Point out each leukocyte.
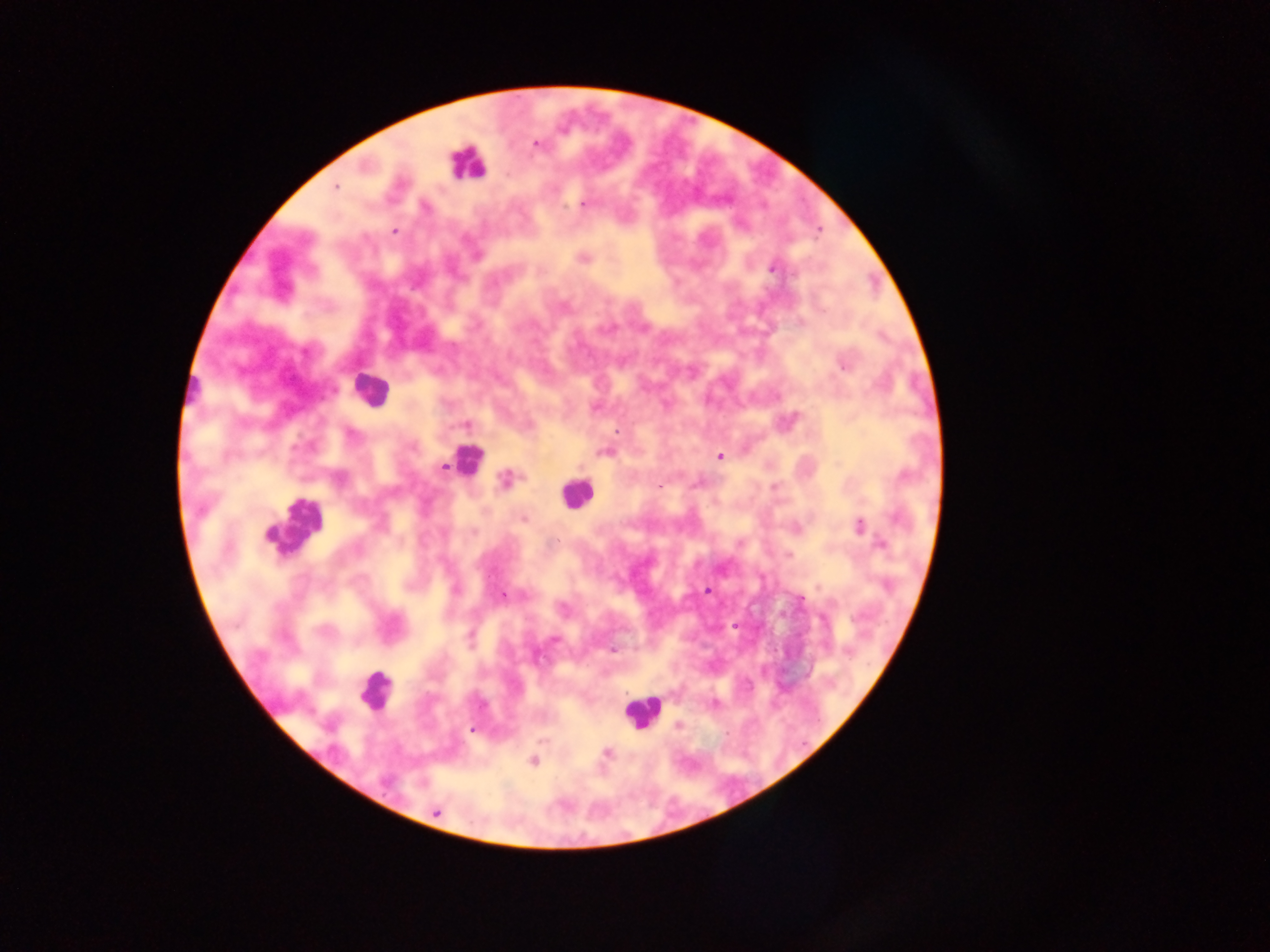

Approximate centers as {x, y} in pixels.
Leukocytes: {467, 163}, {371, 391}, {466, 460}, {575, 493}, {293, 528}, {375, 690}, {642, 712}.

Summary:
  - Plasmodium parasite locations: {536, 143}, {334, 187}, {582, 203}, {394, 231}, {477, 255}, {583, 257}, {773, 267}, {843, 363}, {595, 408}, {465, 424}, {617, 431}, {604, 451}, {719, 456}, {442, 468}, {506, 480}, {660, 487}, {774, 487}, {523, 518}, {859, 527}, {881, 543}, {708, 590}, {502, 595}, {798, 599}, {554, 639}, {612, 649}, {714, 704}, {677, 725}, {471, 729}, {606, 752}, {533, 760}, {436, 811}
  - Image size: 1270×952 pixels
  - Country: Ghana
  - Preparation: thick blood film
  - Field of view: single
  - Capture: mobile-phone photograph through a microscope